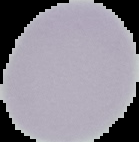 Segmented cell region on a black background. Result: no malaria parasites seen. From a thin blood film. Image is 139×142 pixels.